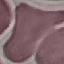

Summary:
  - Malaria status: uninfected
  - Stain: Giemsa
  - Capture: smartphone through the microscope eyepiece
  - Image type: automatically extracted cell patch, resized to 64 × 64 pixels
  - Preparation: thin smear